Assess this cell for malaria.
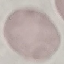
It is uninfected.

Cell patch, automatically extracted from a larger field of view and resized to 64 × 64 pixels. Thin blood film. Giemsa-stained preparation. Acquired by smartphone through the microscope eyepiece.